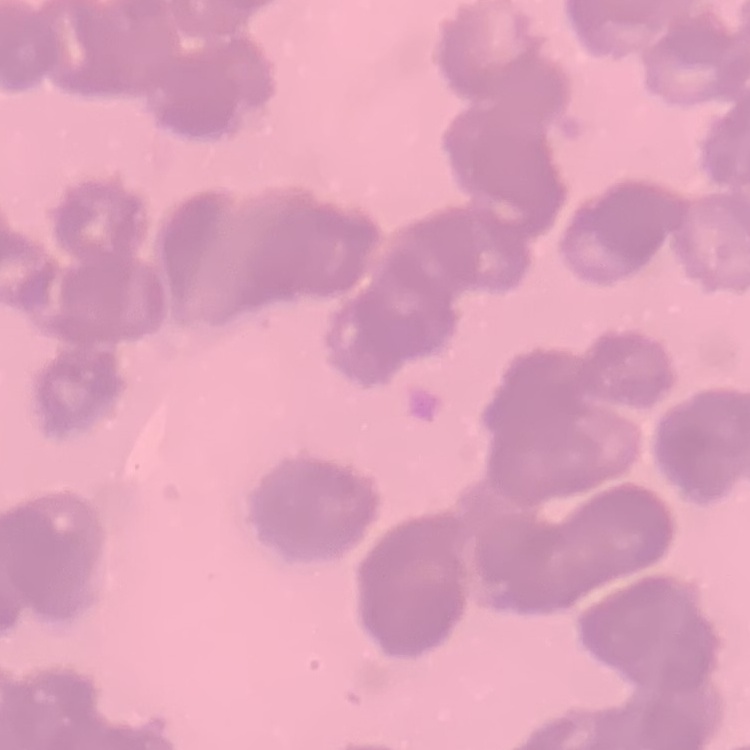

erythrocyte morphology = rouleaux formation
image type = one tile cut from a larger photomicrograph
preparation = thin blood smear
stain = Field's or Giemsa